Report the malaria status of this cell.
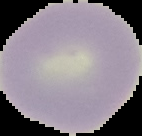

It is uninfected.

Summary:
  - Image type: cell region segmented out of the field of view; surrounding area masked to black
  - Image size: 142×136 pixels
  - Preparation: thin blood film